Describe the morphology of the red blood cells.
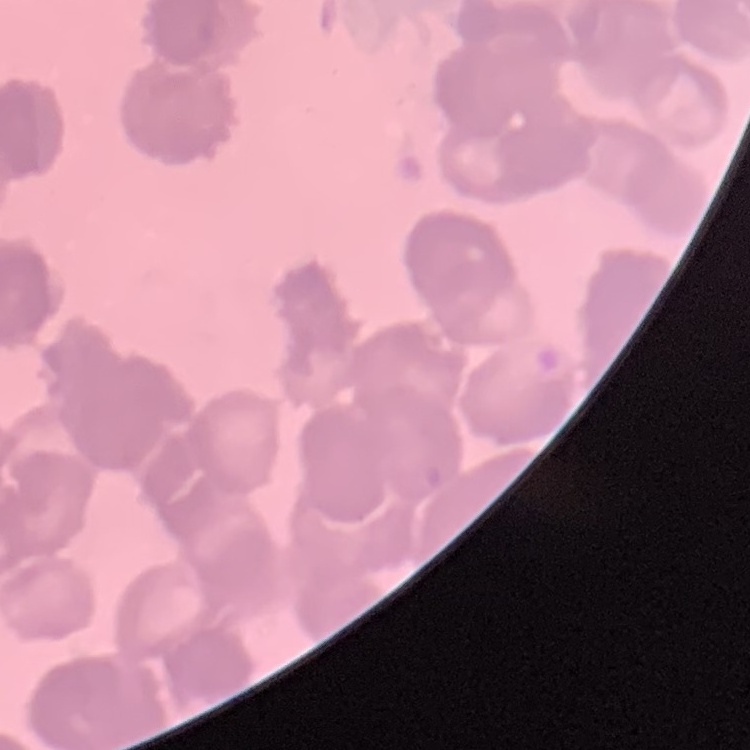
They show rouleaux formation.

Stained with either Field's or Giemsa. Thin blood film. Square crop of a larger photomicrograph.